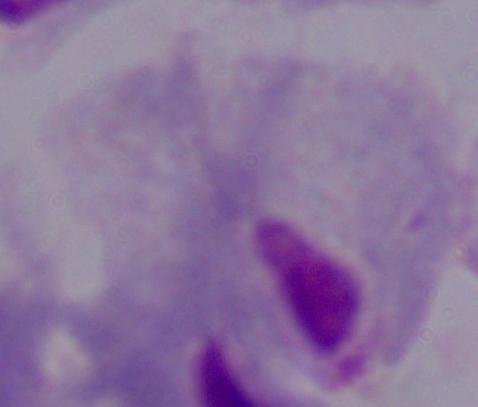
Photomicrograph. 1000x magnification. A trichomonad is shown.